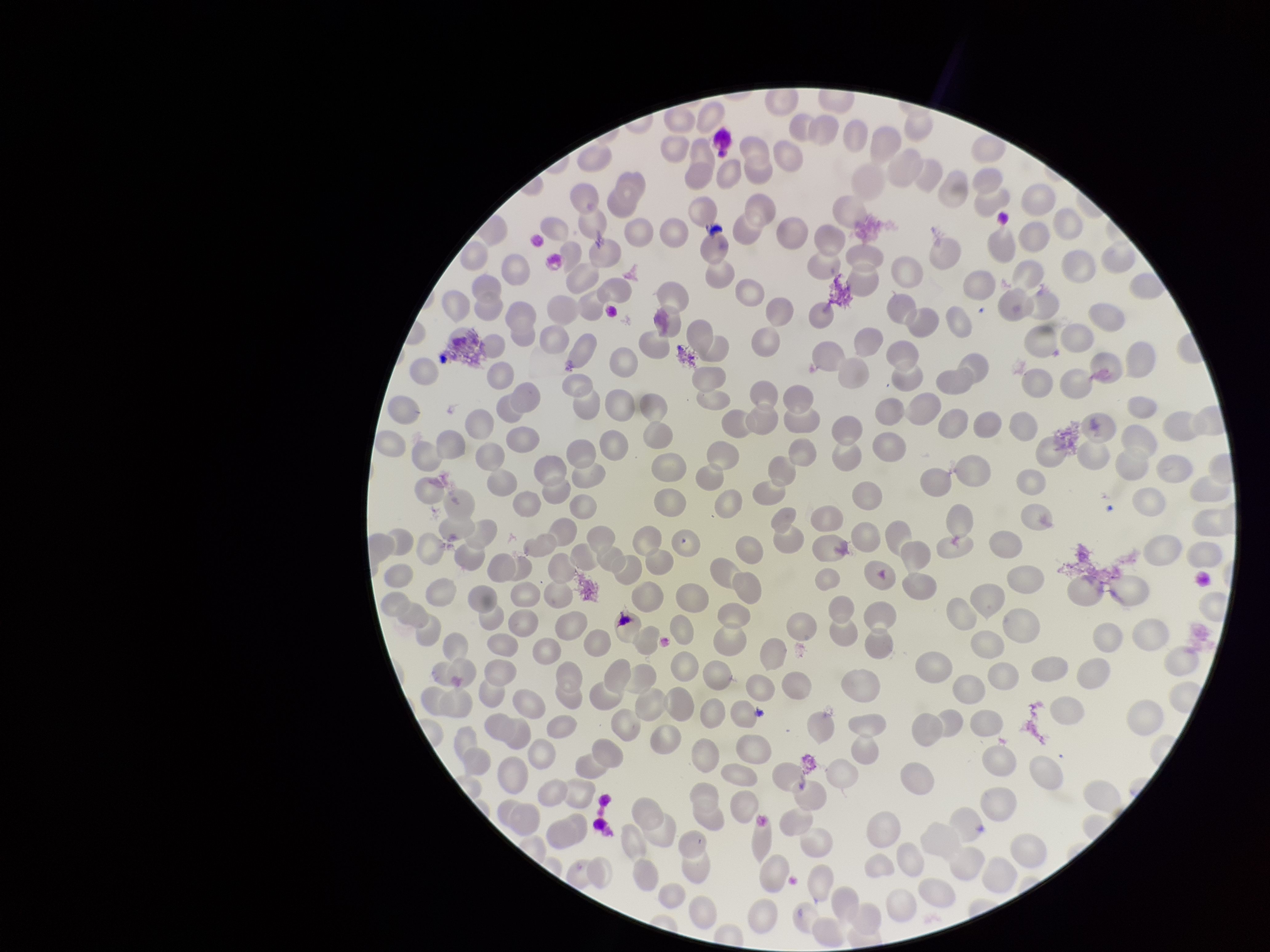
patient_malaria_status: negative
red_blood_cell_count: 254
capture: smartphone photograph through the microscope eyepiece
field_of_view: single
stain: Giemsa
image_size: 1270×952 pixels
preparation: thin blood smear
parasitized_red_blood_cell_count: 0
parasitized_red_blood_cells: none identified